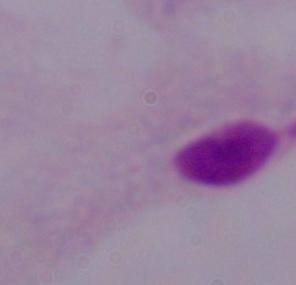
A trichomonad is shown. Photomicrograph. 1000x magnification.